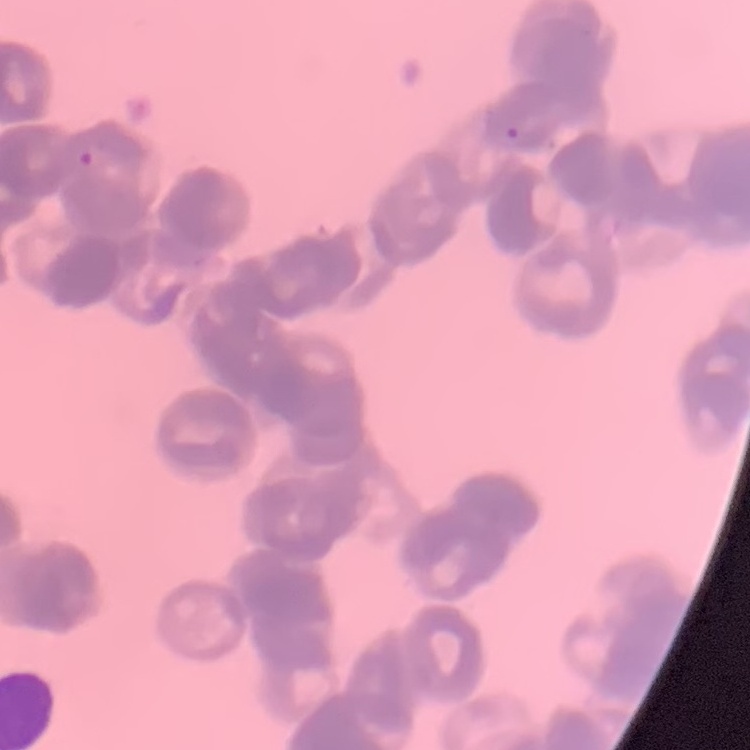
Summary:
  - Erythrocyte morphology: rouleaux formation
  - Stain: Field's or Giemsa
  - Image type: square crop of a larger photomicrograph
  - Preparation: thin peripheral smear